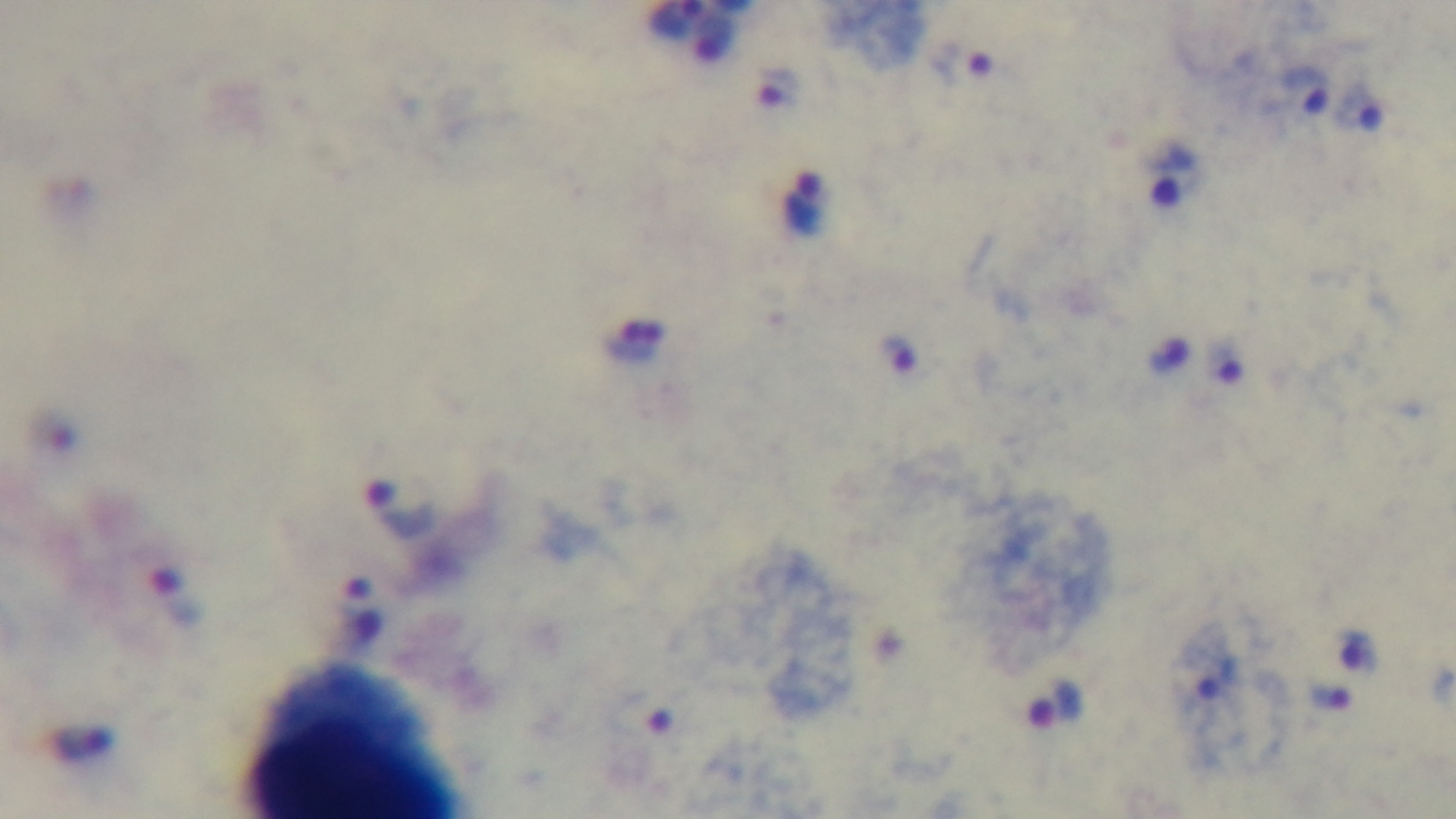

Summary:
  - Objective: 100x oil immersion
  - Modality: light microscopy
  - Preparation: thick smear
  - Stain: Giemsa
  - Capture: mounted 4K digital camera
  - Field of view: one from the slide
  - Malaria status: positive